Give the extent of all Plasmodium falciparum-infected red blood cells.
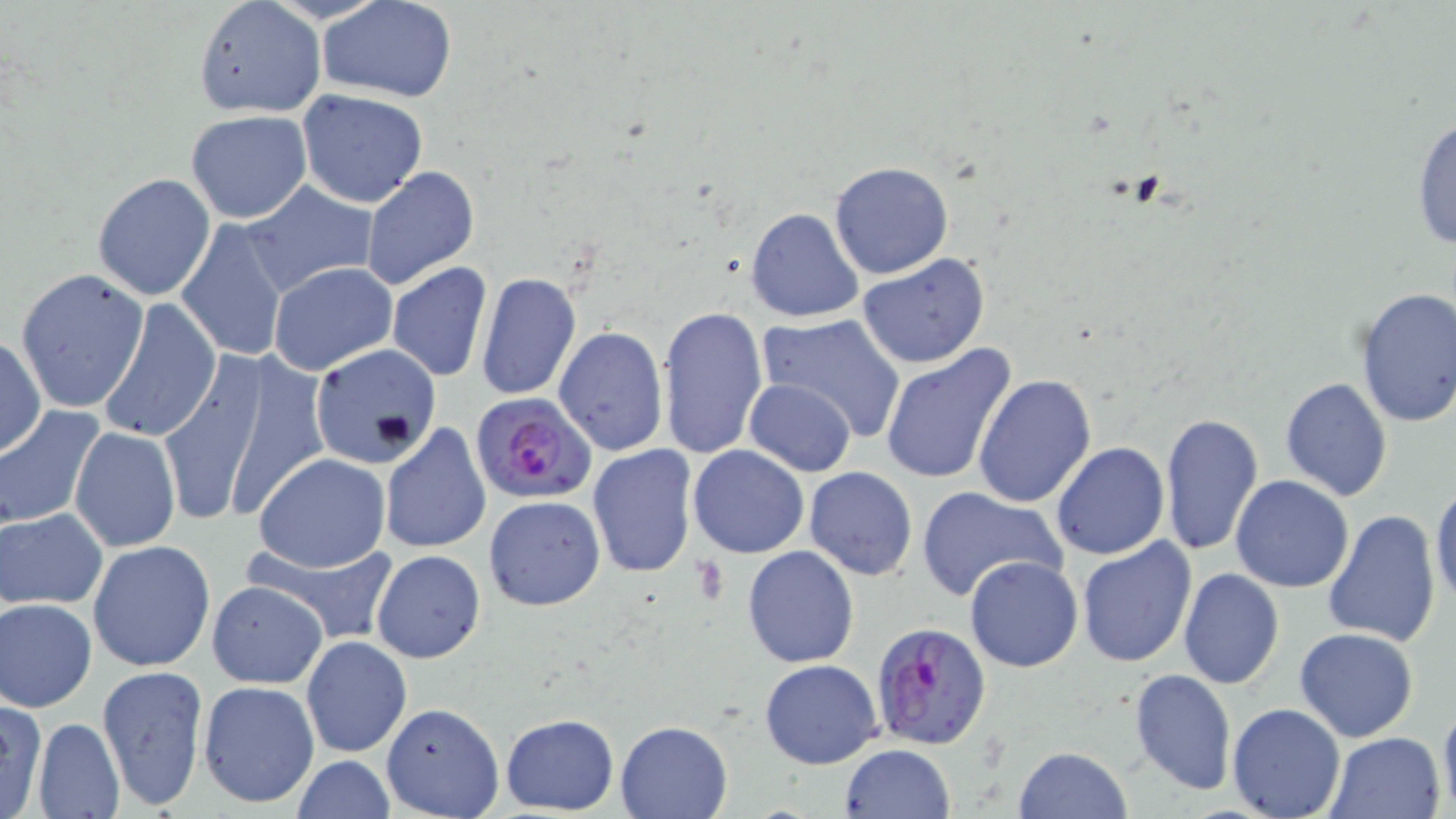
Approximate bounding boxes as (x1, y1, x2, y2) in pixels.
Plasmodium falciparum-infected red blood cells: (472, 393, 598, 507), (870, 623, 993, 751).

Uninfected red blood cell locations: (316, 0, 458, 101), (194, 2, 323, 119), (296, 89, 430, 208), (186, 109, 312, 222), (1410, 111, 1456, 256), (829, 161, 955, 280), (361, 166, 480, 289), (92, 172, 215, 301), (242, 181, 379, 294), (744, 205, 866, 324), (175, 217, 288, 363), (855, 253, 991, 369), (387, 261, 492, 381), (268, 262, 398, 375), (14, 267, 149, 414), (476, 272, 581, 400), (1353, 286, 1456, 429), (99, 297, 221, 443), (658, 305, 768, 460), (755, 314, 907, 439), (554, 325, 668, 454), (0, 335, 46, 459), (880, 343, 1017, 487), (309, 346, 440, 467), (155, 352, 312, 527), (971, 373, 1096, 508), (1279, 375, 1393, 503), (745, 378, 858, 476), (0, 404, 106, 530), (1159, 412, 1263, 558), (379, 422, 490, 555), (68, 426, 182, 552), (1051, 441, 1170, 561), (588, 443, 698, 578), (687, 444, 809, 559), (252, 452, 390, 573), (918, 463, 1159, 583), (804, 466, 918, 579), (1231, 474, 1354, 594), (1431, 482, 1455, 612), (915, 485, 1065, 603), (483, 494, 607, 610), (1, 508, 106, 609), (1322, 508, 1440, 650), (1074, 535, 1198, 669), (247, 538, 400, 642), (88, 540, 215, 672), (741, 545, 858, 668), (372, 550, 487, 663), (965, 555, 1083, 672), (1177, 567, 1285, 691), (206, 580, 328, 688), (2, 597, 97, 713), (1293, 627, 1420, 743), (301, 635, 411, 757), (759, 659, 882, 769), (97, 664, 208, 810), (1127, 669, 1237, 797), (198, 679, 320, 811), (0, 696, 49, 819), (1438, 701, 1456, 815), (380, 702, 504, 818), (1227, 702, 1344, 818), (499, 713, 619, 815), (34, 718, 125, 818), (616, 720, 732, 818), (1324, 730, 1447, 818), (837, 743, 956, 819), (1012, 746, 1132, 819), (290, 754, 396, 819). Slide-level diagnosis: Plasmodium falciparum. Thin blood smear. Image is 1456×819 pixels. 1000x magnification. Light microscopy. One field of a larger specimen. May-Grünwald-Giemsa stain.